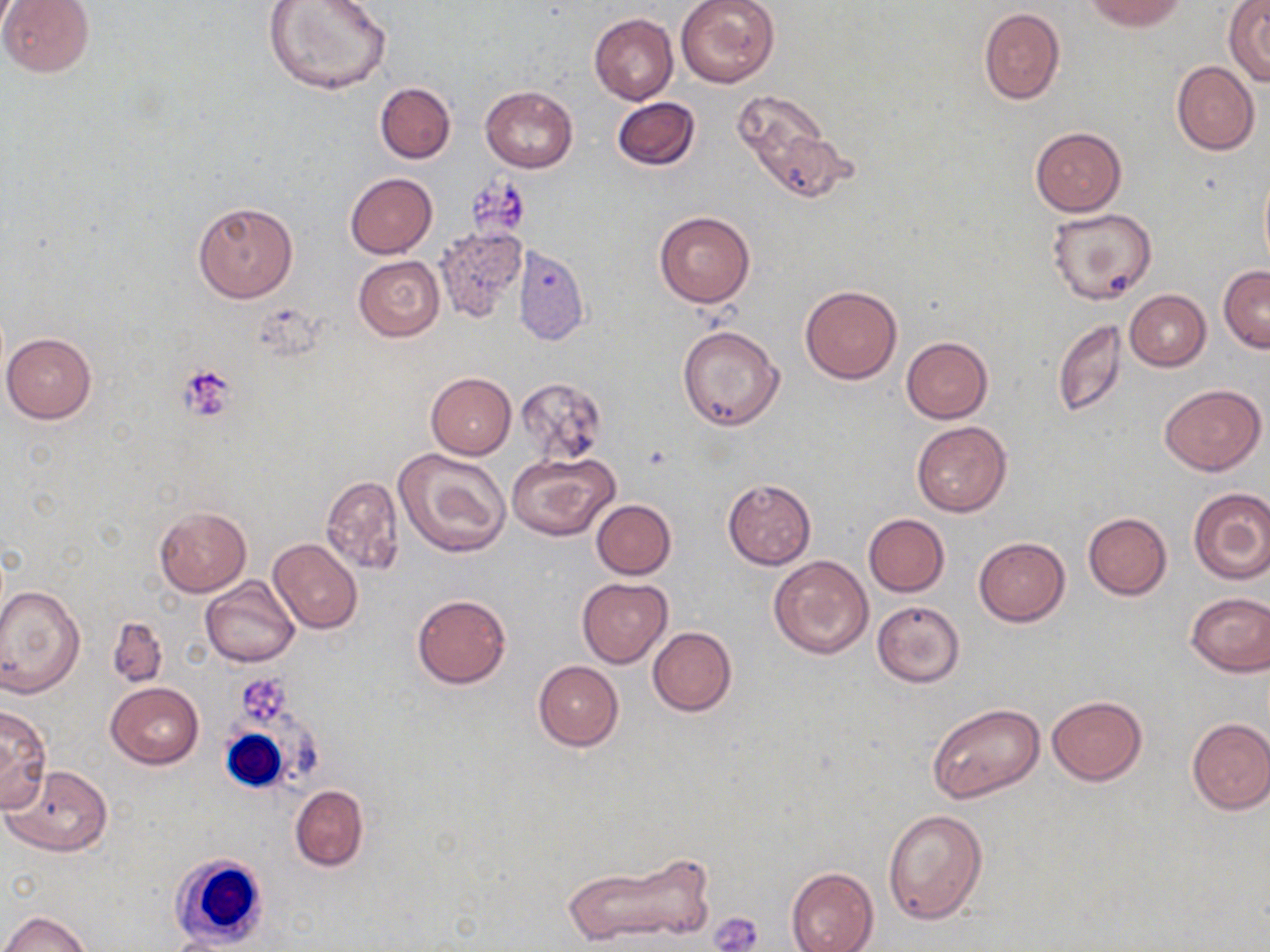
Approximate bounding boxes as (x1, y1, x2, y2) in pixels. Uninfected red blood cell locations: (0, 0, 94, 78), (675, 0, 779, 88), (1082, 0, 1189, 31), (263, 1, 391, 96), (1225, 2, 1270, 83), (978, 7, 1066, 105), (589, 14, 678, 104), (1171, 61, 1259, 155), (376, 82, 456, 163), (481, 85, 577, 172), (732, 90, 838, 196), (611, 96, 701, 170), (1029, 126, 1127, 215), (1259, 168, 1270, 274), (344, 173, 438, 258), (193, 200, 299, 302), (1046, 209, 1157, 306), (655, 211, 754, 308), (434, 225, 528, 323), (514, 245, 589, 344), (354, 256, 444, 341), (1218, 266, 1270, 353), (800, 284, 902, 384), (1125, 289, 1211, 370), (1051, 320, 1128, 418), (677, 324, 786, 431), (2, 333, 97, 424), (901, 336, 993, 422), (426, 372, 517, 460), (514, 377, 607, 462), (1161, 383, 1265, 475), (911, 420, 1012, 517), (393, 448, 512, 558), (507, 452, 620, 542), (321, 476, 404, 574), (722, 478, 816, 570), (1188, 487, 1270, 584), (591, 499, 677, 578), (153, 506, 251, 596), (1083, 512, 1172, 599), (863, 513, 949, 596), (974, 536, 1070, 626), (268, 538, 362, 633), (768, 554, 875, 660), (200, 577, 300, 667), (577, 578, 673, 668), (0, 582, 86, 698), (1185, 592, 1270, 676), (412, 593, 511, 689), (871, 600, 966, 688), (107, 616, 167, 688), (648, 626, 737, 715), (533, 660, 624, 751), (106, 682, 203, 769), (1046, 695, 1149, 785), (0, 703, 53, 813), (927, 704, 1045, 806), (1186, 717, 1270, 814), (3, 765, 113, 856), (290, 785, 369, 871), (882, 807, 988, 924), (564, 850, 715, 947), (787, 866, 878, 952), (2, 910, 91, 952). Platelet locations: (463, 173, 530, 244), (176, 365, 238, 423), (240, 676, 290, 722), (710, 909, 764, 952). White blood cell locations: (217, 713, 326, 788), (166, 854, 263, 946). Slide-level diagnosis: no evidence of blood parasites. May-Grünwald-Giemsa stain. 1000x magnification. Image is 1270×952 pixels. Thin blood smear. One field of a larger specimen. Optical microscopy.